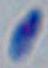

Summary:
  - Identification: Toxoplasma gondii
  - Magnification: 1000x
  - Modality: photomicrograph